Report the malaria status of this cell.
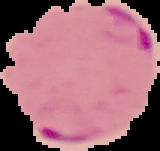

It is parasitized.

Image is 160×151 pixels. From a thin blood smear. Cell region segmented out of the field of view; the surrounding area is masked to black.